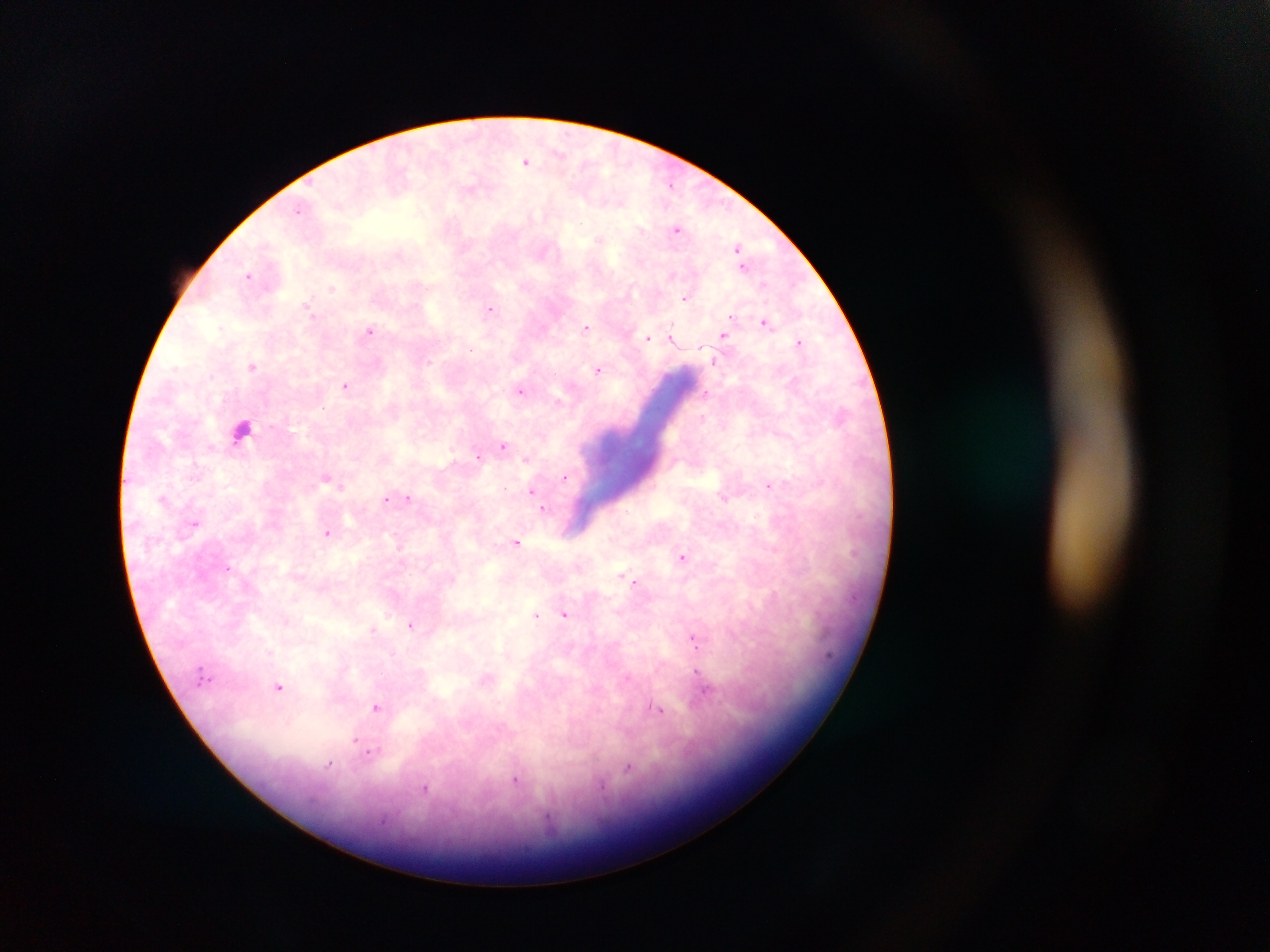

Approximate centers as {x, y} in pixels.
Summary:
  - Leukocyte locations: {242, 428}
  - Plasmodium parasite locations: {527, 161}, {670, 183}, {299, 207}, {677, 229}, {736, 248}, {247, 274}, {332, 287}, {686, 297}, {308, 303}, {491, 309}, {733, 316}, {766, 323}, {586, 327}, {369, 330}, {672, 336}, {724, 336}, {646, 338}, {798, 342}, {428, 361}, {715, 362}, {252, 366}, {598, 369}, {345, 386}, {519, 390}, {505, 446}, {478, 453}, {526, 460}, {327, 478}, {566, 478}, {770, 485}, {530, 493}, {165, 497}, {408, 498}, {385, 500}, {544, 508}, {195, 525}, {328, 532}, {518, 543}, {400, 547}, {683, 557}, {634, 581}, {565, 613}, {535, 615}, {411, 624}, {374, 629}, {694, 638}, {697, 669}, {279, 688}, {707, 692}, {377, 708}, {660, 709}, {355, 741}, {372, 750}, {330, 765}, {628, 770}, {517, 780}, {424, 789}
  - Field of view: single
  - Image size: 1270×952 pixels
  - Capture: mobile-phone photograph through a microscope
  - Preparation: thick blood film
  - Country: Ghana